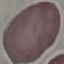

result = negative for malaria parasites
stain = Giemsa
capture = smartphone through the microscope eyepiece
image type = automatically extracted cell patch, resized to 64 × 64 pixels
preparation = thin smear